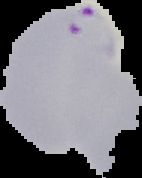

Summary:
  - Image size: 142×178 pixels
  - Preparation: thin blood film
  - Image type: segmented cell region with the area outside set to black
  - Malaria status: parasitized